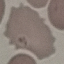
Malaria status: uninfected. Acquired by smartphone through the microscope eyepiece. Thin blood film. Giemsa-stained preparation. Automatically extracted cell patch, resized to 64 × 64 pixels.